Locate and identify every blood parasite.
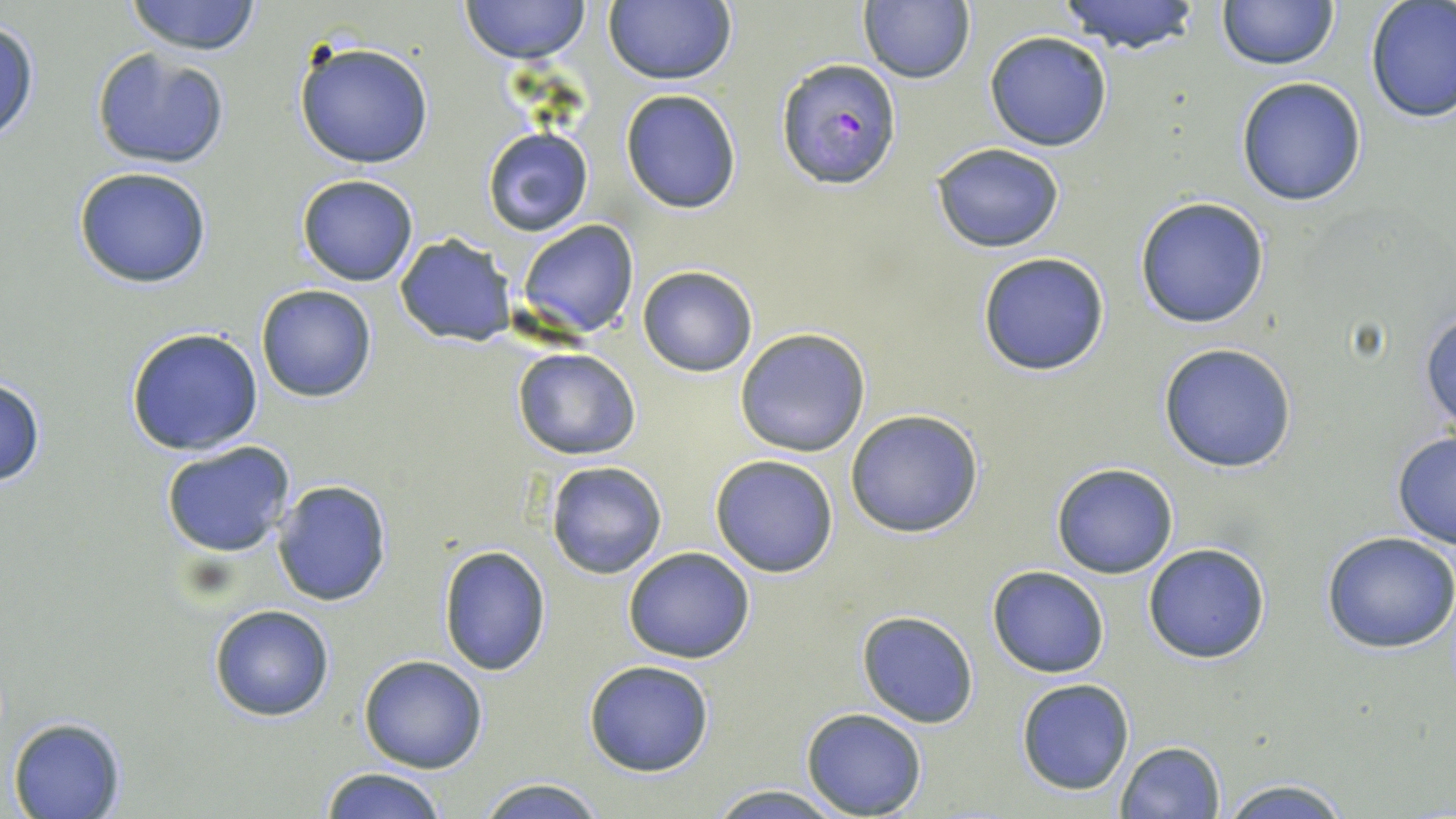
Approximate bounding boxes as (x1, y1, x2, y2) in pixels.
Plasmodium falciparum-infected red blood cells: (777, 57, 903, 189).
No Plasmodium ovale, Plasmodium malariae, Plasmodium vivax, Babesia divergens, or Trypanosoma brucei observed.

slide-level diagnosis = Plasmodium falciparum
preparation = thin blood film
stain = May-Grünwald-Giemsa
modality = light microscopy
image size = 1456×819 pixels
field of view = single
uninfected red blood cell locations = approximate bounding boxes as (x1, y1, x2, y2) in pixels: (124, 0, 262, 55), (458, 0, 592, 65), (1057, 0, 1204, 55), (1218, 1, 1337, 70), (603, 2, 737, 86), (859, 2, 975, 84), (1364, 3, 1456, 124), (1, 19, 40, 146), (984, 30, 1114, 151), (293, 41, 434, 169), (92, 48, 229, 170), (1236, 77, 1367, 206), (620, 89, 742, 213), (481, 127, 595, 237), (933, 142, 1066, 253), (73, 165, 212, 289), (297, 174, 418, 287), (1134, 197, 1270, 329), (516, 219, 639, 336), (395, 235, 515, 347), (976, 251, 1111, 378), (637, 266, 758, 377), (256, 284, 379, 403), (1421, 311, 1456, 432), (125, 326, 264, 456), (734, 328, 871, 457), (1157, 343, 1298, 472), (512, 348, 641, 460), (0, 378, 47, 489), (843, 409, 986, 539), (1391, 432, 1456, 548), (160, 441, 297, 556), (709, 454, 839, 577), (545, 460, 667, 579), (1051, 462, 1179, 578), (273, 479, 394, 608), (1321, 530, 1456, 654), (1142, 542, 1272, 664), (438, 544, 553, 678), (622, 547, 755, 664), (986, 565, 1110, 678), (209, 603, 335, 722), (857, 610, 981, 729), (359, 655, 489, 773), (583, 659, 715, 776), (1016, 678, 1135, 795), (801, 707, 927, 817), (6, 715, 127, 819), (1115, 741, 1228, 819), (319, 767, 445, 819), (475, 777, 604, 817), (1217, 778, 1351, 818), (704, 785, 850, 818)
magnification = 1000x